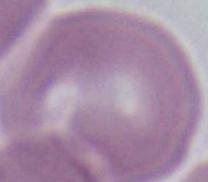
Summary:
  - Modality: photomicrograph
  - Identification: erythrocyte
  - Magnification: 1000x